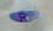
Toxoplasma gondii is seen. Micrograph. Captured at 1000x magnification.